Give the position of every malaria parasite.
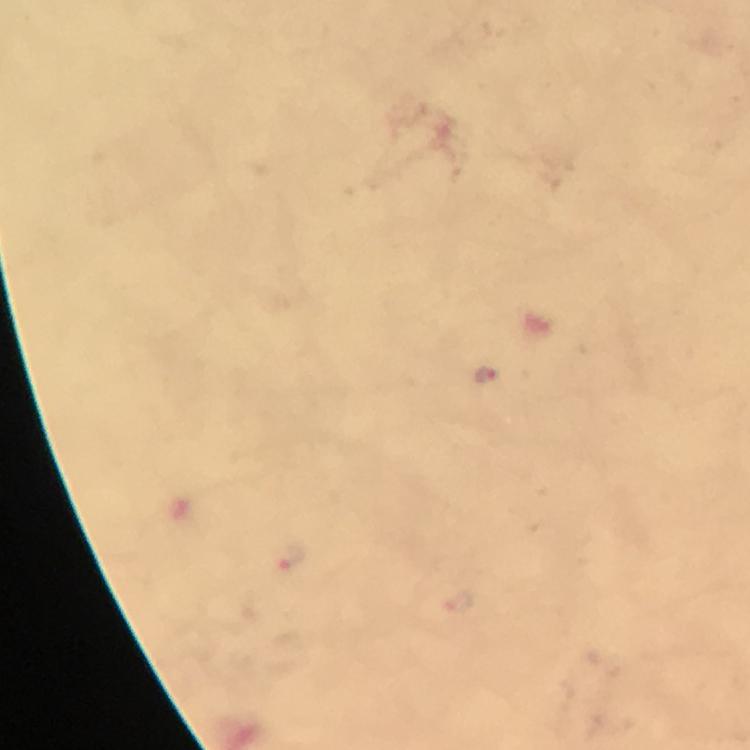
Approximate centers as (x, y) in pixels.
Malaria parasites: (487, 374), (292, 557), (458, 604).

preparation = thick blood smear
cropped from = a single field of view
image size = 750×750 pixels
capture = smartphone photograph through a microscope
immersion oil = applied
stain = Giemsa
magnification = 100x
context = from a malaria diagnostic workup